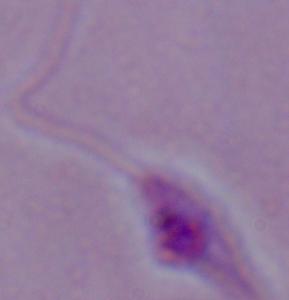

{
  "identification": "Leishmania",
  "magnification": "1000x",
  "modality": "photomicrograph"
}